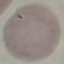 Malaria status: uninfected. Photographed with a smartphone camera at the microscope eyepiece. Thin smear of blood. Automatically extracted cell patch, resized to 64 × 64 pixels. Giemsa-stained preparation.